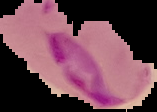
preparation = thin blood smear
image size = 157×112 pixels
result = Plasmodium parasites identified
image type = segmented cell region with the area outside set to black